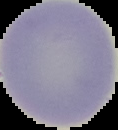

Summary:
  - Image size: 118×130 pixels
  - Preparation: thin blood film
  - Image type: cell region segmented out of the field of view; surrounding area masked to black
  - Malaria status: uninfected